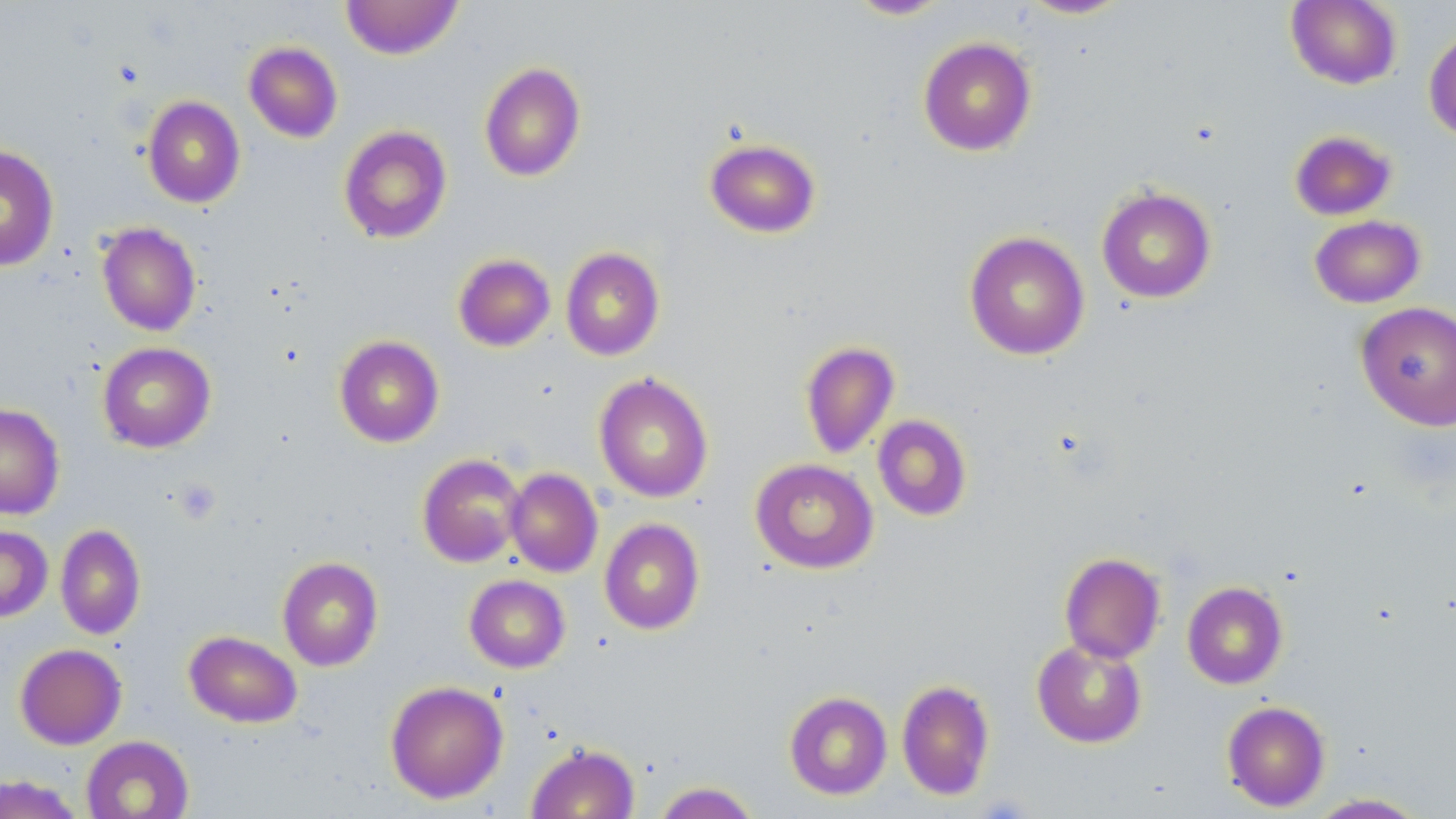

{
  "slide_level_diagnosis": "negative for blood parasites",
  "uninfected_red_blood_cell_locations": "approximate bounding boxes as named x1/y1/x2/y2 corners in pixels: (x1=340, y1=0, x2=464, y2=59), (x1=845, y1=0, x2=953, y2=20), (x1=1016, y1=0, x2=1135, y2=19), (x1=1286, y1=0, x2=1402, y2=89), (x1=1424, y1=25, x2=1456, y2=142), (x1=917, y1=36, x2=1037, y2=156), (x1=243, y1=41, x2=343, y2=143), (x1=479, y1=62, x2=586, y2=182), (x1=142, y1=96, x2=245, y2=208), (x1=338, y1=125, x2=452, y2=244), (x1=1289, y1=129, x2=1397, y2=220), (x1=704, y1=137, x2=821, y2=238), (x1=0, y1=145, x2=59, y2=271), (x1=1096, y1=186, x2=1217, y2=303), (x1=1309, y1=214, x2=1426, y2=308), (x1=96, y1=222, x2=201, y2=336), (x1=964, y1=231, x2=1090, y2=361), (x1=560, y1=247, x2=665, y2=361), (x1=453, y1=253, x2=555, y2=352), (x1=1355, y1=301, x2=1456, y2=430), (x1=334, y1=335, x2=444, y2=447), (x1=799, y1=340, x2=899, y2=458), (x1=98, y1=342, x2=216, y2=453), (x1=593, y1=372, x2=714, y2=503), (x1=0, y1=403, x2=65, y2=520), (x1=872, y1=414, x2=972, y2=521), (x1=417, y1=453, x2=527, y2=567), (x1=750, y1=458, x2=878, y2=574), (x1=505, y1=467, x2=603, y2=577), (x1=599, y1=518, x2=705, y2=635), (x1=55, y1=523, x2=146, y2=640), (x1=0, y1=525, x2=53, y2=622), (x1=1059, y1=552, x2=1166, y2=663), (x1=277, y1=556, x2=384, y2=671), (x1=464, y1=575, x2=570, y2=673), (x1=1182, y1=581, x2=1288, y2=689), (x1=184, y1=630, x2=302, y2=728), (x1=1031, y1=638, x2=1147, y2=748), (x1=14, y1=643, x2=127, y2=749), (x1=896, y1=679, x2=995, y2=800), (x1=385, y1=681, x2=508, y2=804), (x1=784, y1=691, x2=892, y2=800), (x1=1221, y1=700, x2=1331, y2=811), (x1=81, y1=735, x2=194, y2=819), (x1=526, y1=743, x2=640, y2=819), (x1=0, y1=774, x2=85, y2=819), (x1=653, y1=781, x2=761, y2=819), (x1=1305, y1=792, x2=1429, y2=818)",
  "field_of_view": "single",
  "stain": "May-Grünwald-Giemsa",
  "magnification": "1000x",
  "image_size": "1456×819 pixels",
  "preparation": "thin blood smear",
  "platelet_locations": "approximate bounding boxes as named x1/y1/x2/y2 corners in pixels: (x1=175, y1=479, x2=221, y2=524)",
  "modality": "optical microscopy"
}